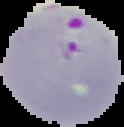

preparation = thin blood smear
image size = 124×127 pixels
result = malaria parasites detected
image type = cell region segmented out of the field of view; surrounding area masked to black